Report the malaria status of this cell.
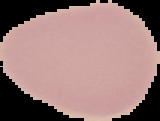

It is uninfected.

image size = 160×121 pixels
preparation = thin blood smear
image type = segmented cell region on a black background